Name the parasite shown.
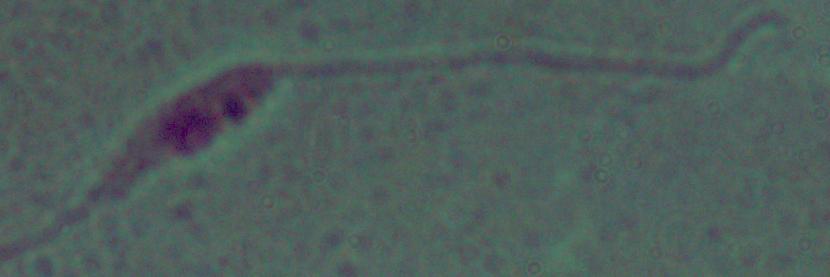
Leishmania.

Summary:
  - Modality: micrograph
  - Magnification: 1000x